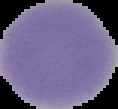

result = no malaria parasites detected
preparation = thin blood smear
image size = 118×109 pixels
image type = segmented cell region with the area outside set to black